Classify this cell by malaria status.
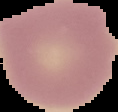

It is uninfected.

The area outside the segmented cell region is set to black. From a thin blood smear. Image is 118×112 pixels.